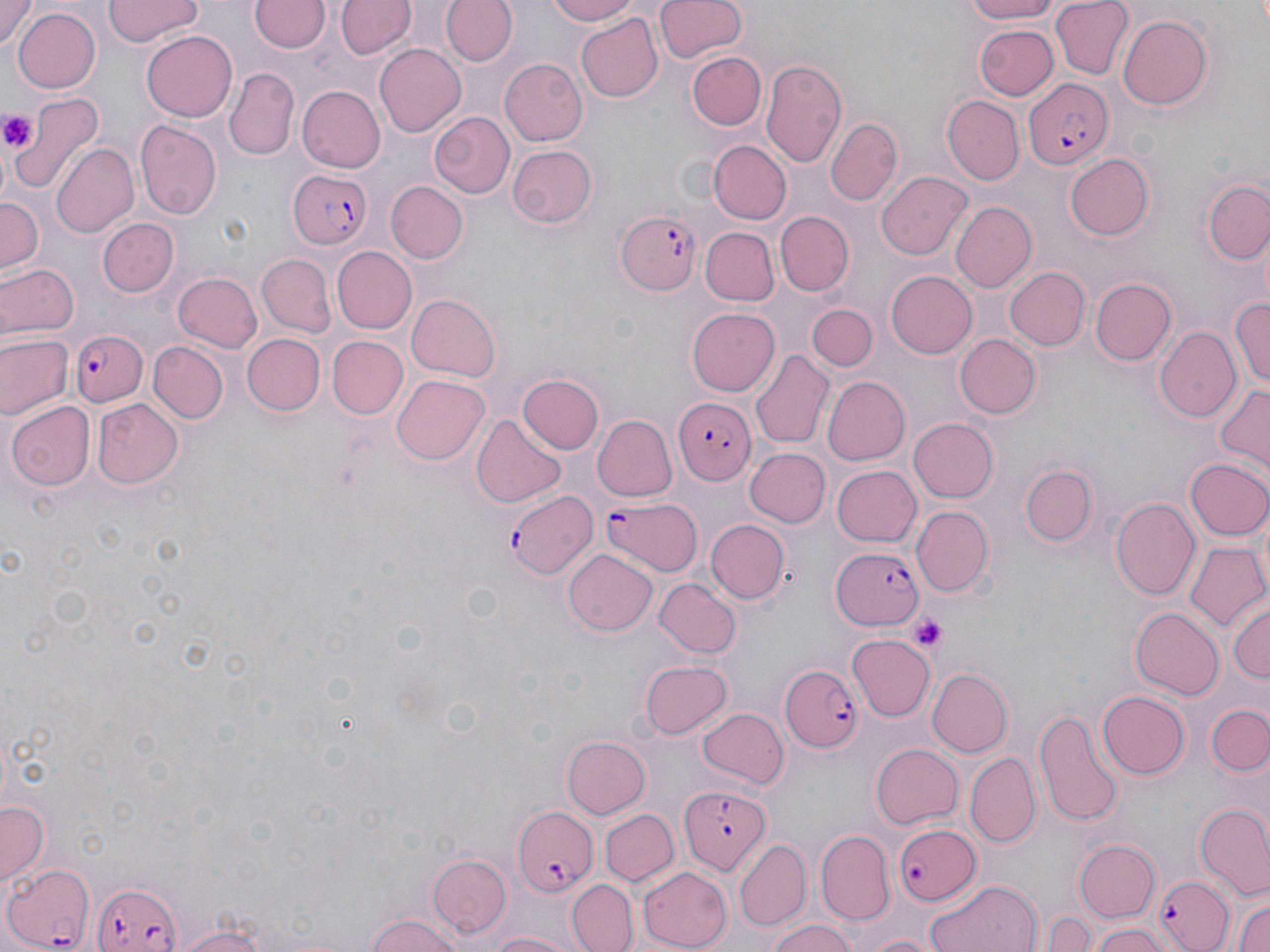

slide-level diagnosis = Plasmodium falciparum
image size = 1270×952 pixels
platelet locations = approximate bounding boxes as named x1/y1/x2/y2 corners in pixels: (x1=0, y1=109, x2=37, y2=155), (x1=911, y1=615, x2=947, y2=654)
preparation = thin blood film
uninfected red blood cell locations = approximate bounding boxes as named x1/y1/x2/y2 corners in pixels: (x1=1, y1=0, x2=37, y2=50), (x1=103, y1=0, x2=202, y2=48), (x1=441, y1=0, x2=517, y2=67), (x1=544, y1=0, x2=646, y2=25), (x1=654, y1=0, x2=746, y2=63), (x1=956, y1=0, x2=1066, y2=24), (x1=1049, y1=0, x2=1132, y2=80), (x1=251, y1=1, x2=327, y2=53), (x1=334, y1=1, x2=413, y2=60), (x1=11, y1=8, x2=100, y2=92), (x1=1117, y1=12, x2=1213, y2=107), (x1=577, y1=14, x2=665, y2=102), (x1=974, y1=24, x2=1058, y2=100), (x1=141, y1=31, x2=236, y2=120), (x1=374, y1=43, x2=466, y2=137), (x1=687, y1=51, x2=766, y2=133), (x1=499, y1=58, x2=588, y2=147), (x1=760, y1=59, x2=847, y2=171), (x1=224, y1=69, x2=297, y2=159), (x1=296, y1=85, x2=385, y2=173), (x1=10, y1=93, x2=104, y2=193), (x1=943, y1=94, x2=1024, y2=183), (x1=428, y1=109, x2=514, y2=200), (x1=826, y1=118, x2=902, y2=204), (x1=137, y1=119, x2=223, y2=222), (x1=710, y1=140, x2=790, y2=224), (x1=50, y1=143, x2=139, y2=238), (x1=507, y1=144, x2=599, y2=230), (x1=1063, y1=151, x2=1155, y2=242), (x1=875, y1=170, x2=971, y2=260), (x1=1200, y1=175, x2=1270, y2=267), (x1=387, y1=182, x2=467, y2=264), (x1=0, y1=195, x2=42, y2=275), (x1=949, y1=201, x2=1036, y2=294), (x1=775, y1=211, x2=855, y2=294), (x1=97, y1=216, x2=179, y2=297), (x1=699, y1=227, x2=779, y2=304), (x1=330, y1=246, x2=416, y2=333), (x1=255, y1=254, x2=335, y2=337), (x1=1, y1=262, x2=78, y2=340), (x1=1005, y1=265, x2=1090, y2=350), (x1=884, y1=270, x2=976, y2=359), (x1=172, y1=272, x2=263, y2=353), (x1=1089, y1=277, x2=1178, y2=366), (x1=407, y1=293, x2=501, y2=378), (x1=1232, y1=295, x2=1270, y2=392), (x1=809, y1=306, x2=877, y2=372), (x1=685, y1=307, x2=781, y2=396), (x1=1154, y1=327, x2=1241, y2=424), (x1=239, y1=332, x2=324, y2=416), (x1=1, y1=333, x2=72, y2=419), (x1=953, y1=333, x2=1040, y2=419), (x1=328, y1=336, x2=408, y2=419), (x1=148, y1=343, x2=225, y2=424), (x1=750, y1=349, x2=834, y2=450), (x1=390, y1=374, x2=490, y2=465), (x1=519, y1=374, x2=604, y2=455), (x1=821, y1=375, x2=910, y2=465), (x1=1213, y1=382, x2=1270, y2=468), (x1=9, y1=399, x2=94, y2=492), (x1=91, y1=400, x2=181, y2=488), (x1=471, y1=413, x2=564, y2=508), (x1=594, y1=414, x2=676, y2=499), (x1=910, y1=417, x2=999, y2=502), (x1=743, y1=448, x2=830, y2=529), (x1=1185, y1=457, x2=1270, y2=540), (x1=1020, y1=463, x2=1097, y2=546), (x1=831, y1=464, x2=922, y2=547), (x1=1111, y1=496, x2=1201, y2=601), (x1=909, y1=504, x2=993, y2=596), (x1=708, y1=519, x2=788, y2=603), (x1=1185, y1=542, x2=1270, y2=631), (x1=563, y1=550, x2=656, y2=636), (x1=655, y1=578, x2=740, y2=659), (x1=1227, y1=601, x2=1269, y2=686), (x1=1130, y1=607, x2=1223, y2=699), (x1=849, y1=636, x2=936, y2=721), (x1=640, y1=657, x2=734, y2=738), (x1=928, y1=667, x2=1013, y2=756), (x1=1096, y1=689, x2=1188, y2=779), (x1=1208, y1=703, x2=1270, y2=777), (x1=696, y1=706, x2=788, y2=790), (x1=1034, y1=707, x2=1123, y2=826), (x1=563, y1=737, x2=650, y2=819), (x1=870, y1=743, x2=963, y2=830), (x1=966, y1=752, x2=1041, y2=848), (x1=0, y1=798, x2=49, y2=884), (x1=1196, y1=806, x2=1270, y2=899), (x1=600, y1=809, x2=679, y2=886), (x1=816, y1=832, x2=894, y2=926), (x1=734, y1=840, x2=810, y2=930), (x1=1073, y1=840, x2=1161, y2=923), (x1=426, y1=851, x2=509, y2=938), (x1=636, y1=867, x2=735, y2=949), (x1=566, y1=876, x2=637, y2=952), (x1=925, y1=881, x2=1044, y2=952), (x1=1230, y1=885, x2=1270, y2=952), (x1=1043, y1=909, x2=1099, y2=951), (x1=363, y1=912, x2=467, y2=952), (x1=765, y1=917, x2=858, y2=952), (x1=1088, y1=921, x2=1169, y2=952), (x1=170, y1=925, x2=273, y2=952), (x1=481, y1=928, x2=583, y2=951), (x1=856, y1=931, x2=946, y2=952)
modality = optical microscopy
magnification = 1000x
stain = May-Grünwald-Giemsa
field of view = one of a larger specimen
Plasmodium falciparum-infected red blood cell locations = approximate bounding boxes as named x1/y1/x2/y2 corners in pixels: (x1=1025, y1=81, x2=1116, y2=169), (x1=287, y1=168, x2=372, y2=251), (x1=613, y1=205, x2=701, y2=301), (x1=70, y1=329, x2=147, y2=407), (x1=677, y1=399, x2=756, y2=483), (x1=505, y1=491, x2=596, y2=581), (x1=598, y1=496, x2=705, y2=578), (x1=831, y1=547, x2=927, y2=630), (x1=779, y1=665, x2=865, y2=752), (x1=678, y1=785, x2=768, y2=875), (x1=512, y1=807, x2=597, y2=893), (x1=890, y1=823, x2=980, y2=904), (x1=3, y1=863, x2=96, y2=951), (x1=1154, y1=872, x2=1234, y2=951), (x1=90, y1=880, x2=184, y2=952)